Locate and identify every blood parasite.
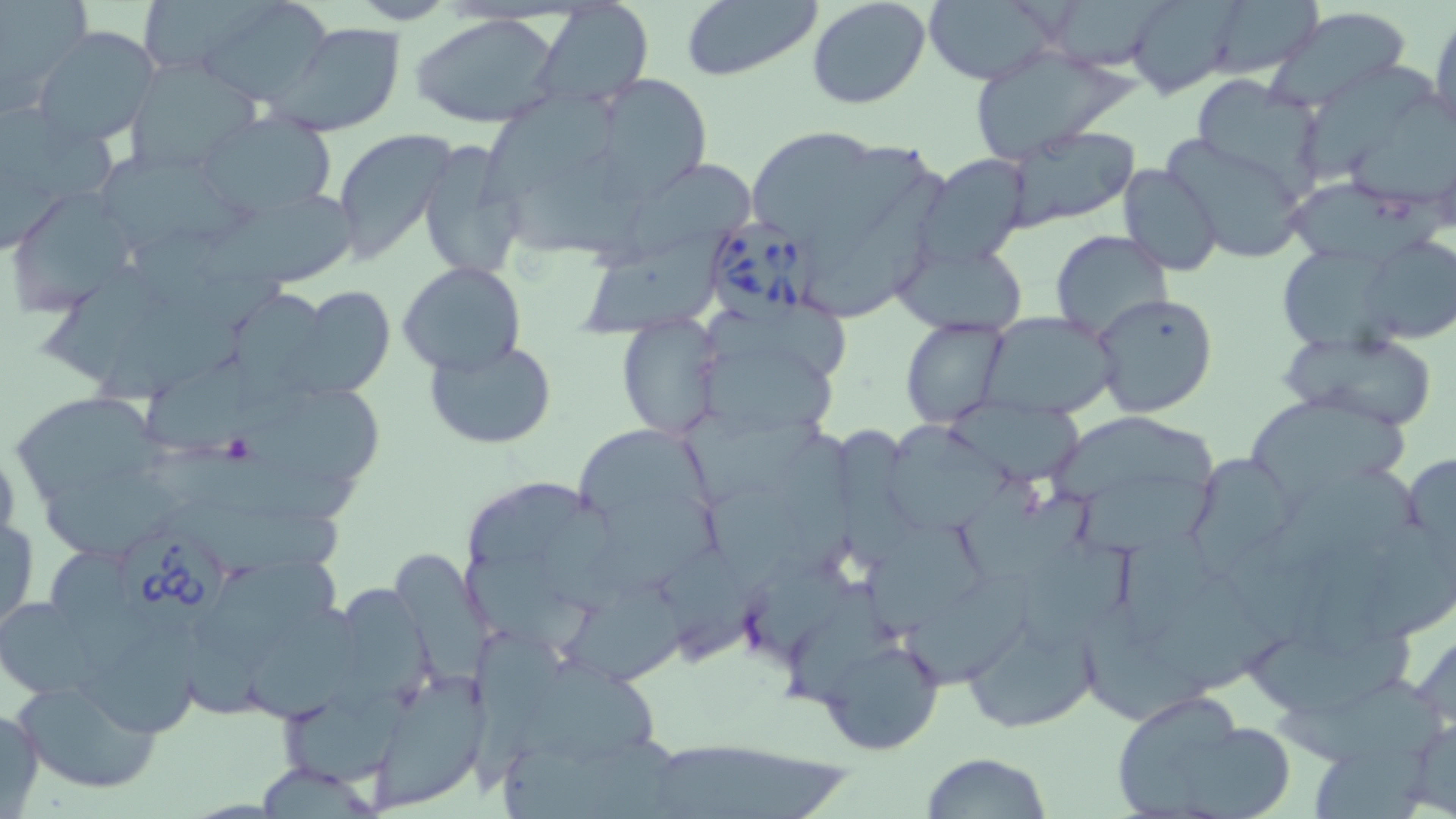
Approximate bounding boxes as named x1/y1/x2/y2 corners in pixels.
Babesia divergens-infected red blood cells: (x1=709, y1=218, x2=824, y2=332), (x1=123, y1=531, x2=237, y2=634).
No Plasmodium falciparum, Plasmodium ovale, Plasmodium malariae, Plasmodium vivax, or Trypanosoma brucei observed.

slide-level diagnosis = Babesia divergens
magnification = 1000x
modality = light microscopy
field of view = single
image size = 1456×819 pixels
platelet locations = approximate bounding boxes as named x1/y1/x2/y2 corners in pixels: (x1=219, y1=433, x2=259, y2=465)
uninfected red blood cell locations = approximate bounding boxes as named x1/y1/x2/y2 corners in pixels: (x1=138, y1=0, x2=262, y2=77), (x1=201, y1=0, x2=335, y2=105), (x1=680, y1=0, x2=823, y2=82), (x1=805, y1=0, x2=931, y2=110), (x1=922, y1=0, x2=1061, y2=85), (x1=1045, y1=0, x2=1173, y2=72), (x1=1126, y1=0, x2=1239, y2=97), (x1=1198, y1=1, x2=1325, y2=80), (x1=0, y1=2, x2=87, y2=104), (x1=535, y1=3, x2=652, y2=110), (x1=1263, y1=6, x2=1413, y2=111), (x1=1429, y1=13, x2=1456, y2=141), (x1=413, y1=15, x2=562, y2=128), (x1=271, y1=20, x2=404, y2=136), (x1=32, y1=26, x2=159, y2=147), (x1=964, y1=44, x2=1142, y2=162), (x1=127, y1=61, x2=261, y2=175), (x1=1305, y1=64, x2=1438, y2=188), (x1=592, y1=72, x2=715, y2=196), (x1=1192, y1=76, x2=1328, y2=196), (x1=479, y1=82, x2=626, y2=217), (x1=1348, y1=95, x2=1456, y2=215), (x1=0, y1=112, x2=125, y2=202), (x1=198, y1=113, x2=336, y2=219), (x1=1004, y1=127, x2=1139, y2=232), (x1=333, y1=128, x2=452, y2=261), (x1=752, y1=134, x2=880, y2=236), (x1=1158, y1=134, x2=1312, y2=262), (x1=417, y1=143, x2=526, y2=282), (x1=810, y1=144, x2=939, y2=284), (x1=99, y1=153, x2=250, y2=249), (x1=914, y1=154, x2=1032, y2=269), (x1=592, y1=160, x2=757, y2=278), (x1=1117, y1=163, x2=1224, y2=275), (x1=805, y1=172, x2=956, y2=321), (x1=1283, y1=178, x2=1456, y2=273), (x1=5, y1=187, x2=138, y2=312), (x1=190, y1=193, x2=362, y2=293), (x1=581, y1=229, x2=733, y2=342), (x1=1050, y1=231, x2=1174, y2=342), (x1=1358, y1=232, x2=1454, y2=344), (x1=892, y1=236, x2=1029, y2=336), (x1=1281, y1=246, x2=1415, y2=360), (x1=397, y1=260, x2=527, y2=377), (x1=299, y1=287, x2=396, y2=396), (x1=230, y1=293, x2=335, y2=414), (x1=1090, y1=293, x2=1219, y2=419), (x1=95, y1=302, x2=256, y2=408), (x1=978, y1=311, x2=1117, y2=419), (x1=616, y1=315, x2=724, y2=440), (x1=901, y1=317, x2=1011, y2=428), (x1=1283, y1=329, x2=1440, y2=431), (x1=426, y1=340, x2=556, y2=449), (x1=699, y1=349, x2=837, y2=439), (x1=9, y1=390, x2=175, y2=505), (x1=1242, y1=390, x2=1412, y2=507), (x1=240, y1=397, x2=393, y2=485), (x1=952, y1=401, x2=1089, y2=492), (x1=675, y1=408, x2=834, y2=507), (x1=1054, y1=417, x2=1239, y2=514), (x1=825, y1=422, x2=929, y2=573), (x1=883, y1=422, x2=1018, y2=541), (x1=581, y1=429, x2=722, y2=539), (x1=0, y1=440, x2=20, y2=559), (x1=157, y1=443, x2=370, y2=526), (x1=1402, y1=450, x2=1456, y2=571), (x1=1184, y1=451, x2=1303, y2=568), (x1=45, y1=468, x2=200, y2=565), (x1=1075, y1=478, x2=1222, y2=564), (x1=469, y1=484, x2=611, y2=577), (x1=952, y1=486, x2=1102, y2=587), (x1=1, y1=510, x2=38, y2=635), (x1=866, y1=519, x2=985, y2=640), (x1=1019, y1=540, x2=1149, y2=662), (x1=395, y1=551, x2=500, y2=695), (x1=200, y1=558, x2=349, y2=665), (x1=332, y1=574, x2=436, y2=717), (x1=784, y1=590, x2=915, y2=719), (x1=565, y1=591, x2=708, y2=699), (x1=3, y1=596, x2=105, y2=699), (x1=1081, y1=603, x2=1218, y2=735), (x1=248, y1=604, x2=365, y2=730), (x1=959, y1=612, x2=1098, y2=732), (x1=71, y1=617, x2=207, y2=744), (x1=1248, y1=621, x2=1424, y2=723), (x1=464, y1=625, x2=608, y2=798), (x1=815, y1=635, x2=946, y2=756), (x1=512, y1=658, x2=673, y2=771), (x1=1276, y1=676, x2=1451, y2=775), (x1=13, y1=677, x2=165, y2=795), (x1=367, y1=677, x2=489, y2=810), (x1=1106, y1=688, x2=1293, y2=819), (x1=282, y1=690, x2=403, y2=788), (x1=0, y1=703, x2=45, y2=817), (x1=1401, y1=713, x2=1456, y2=815), (x1=645, y1=738, x2=857, y2=819), (x1=921, y1=752, x2=1051, y2=819), (x1=251, y1=762, x2=384, y2=816)
stain = May-Grünwald-Giemsa
preparation = thin blood smear